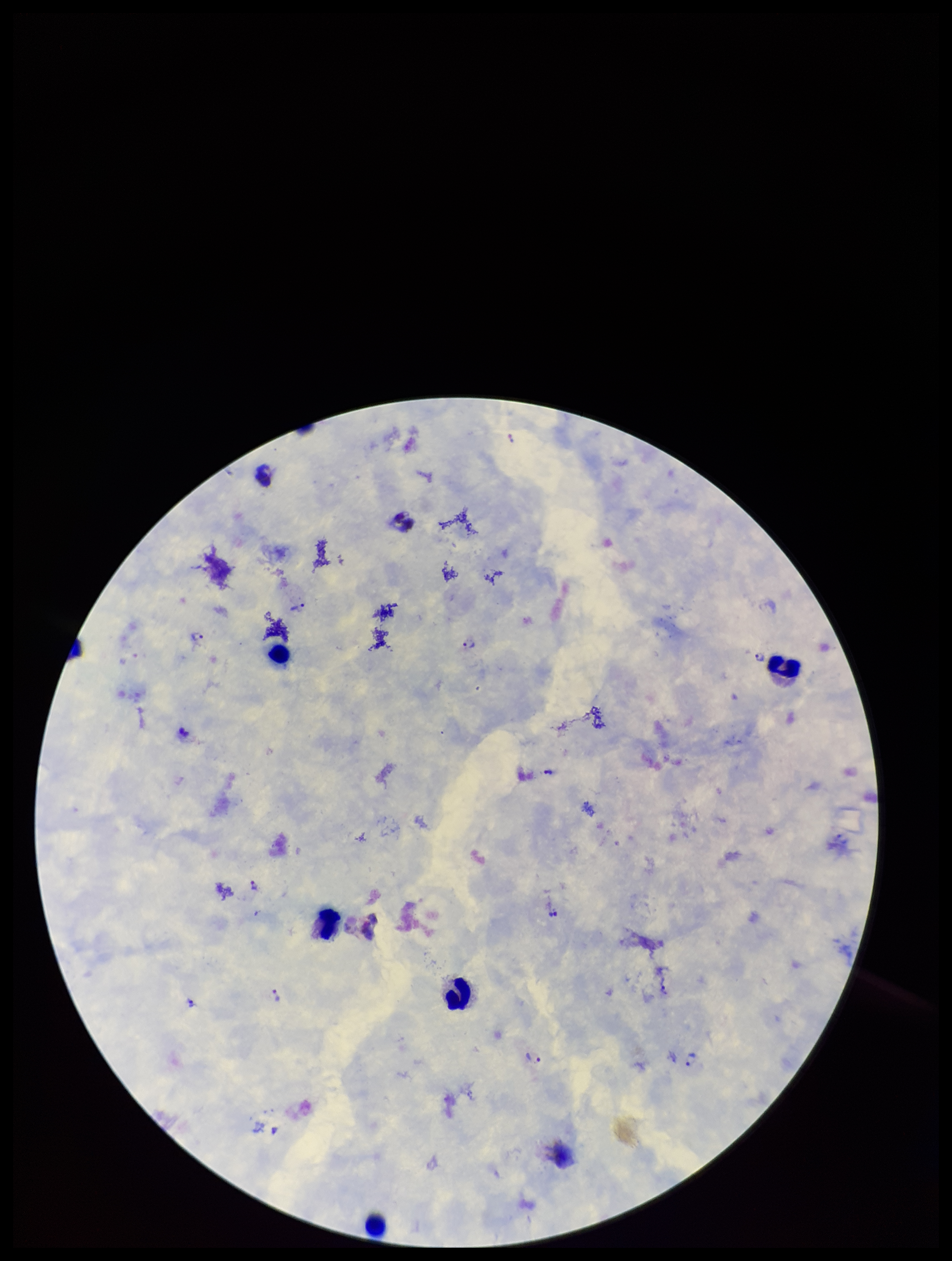
Preparation: thick blood smear. Image is 952×1261 pixels. Giemsa stain. Photographed through the microscope eyepiece with a smartphone camera. Patient malaria status: infected. Species reported for this patient: Plasmodium vivax. Plasmodium parasites: detected. Leukocyte count: 7. Parasite count: 12. One field from this slide.